Locate every blood parasite and identify its species.
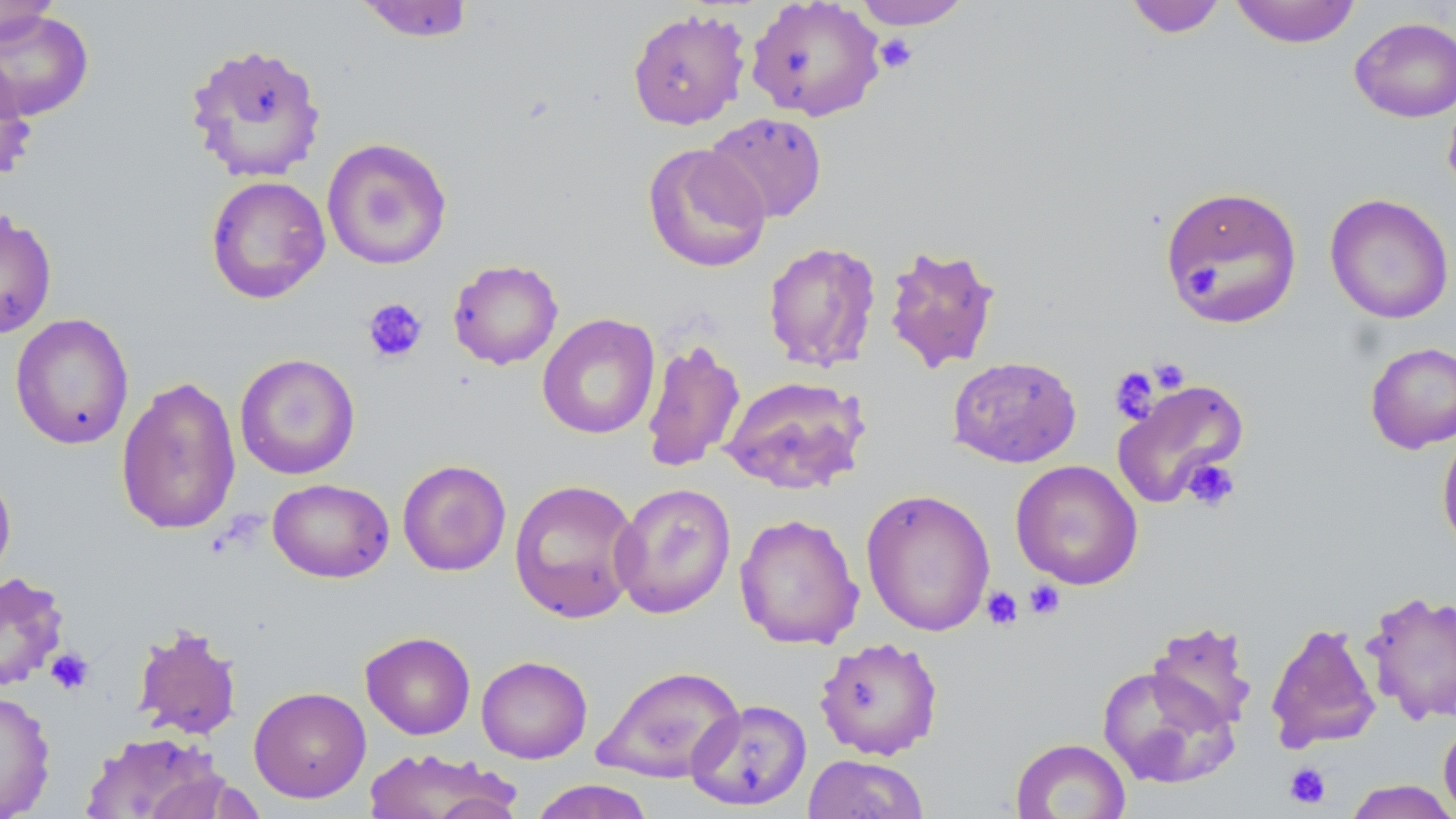

No blood parasites observed.

Summary:
  - Coordinate format: approximate bounding boxes as [x1, y1, x2, y2] in pixels
  - Platelet locations: [874, 33, 918, 74], [1183, 263, 1223, 300], [362, 297, 428, 364], [1149, 357, 1191, 394], [1110, 366, 1161, 424], [1181, 458, 1240, 513], [1024, 579, 1066, 620], [982, 586, 1024, 631], [45, 647, 95, 695], [1284, 762, 1331, 809]
  - Uninfected red blood cell locations: [0, 0, 62, 46], [745, 0, 885, 122], [853, 0, 972, 29], [1124, 0, 1228, 38], [1230, 0, 1361, 48], [355, 1, 477, 42], [0, 8, 95, 122], [627, 8, 751, 130], [1350, 16, 1456, 122], [183, 41, 327, 184], [0, 57, 36, 182], [1442, 92, 1456, 200], [704, 111, 828, 223], [321, 136, 453, 271], [642, 142, 772, 274], [205, 175, 331, 305], [1159, 185, 1303, 328], [1325, 193, 1454, 324], [0, 210, 58, 339], [762, 241, 882, 372], [882, 242, 1001, 374], [448, 259, 563, 370], [10, 313, 134, 450], [537, 313, 659, 440], [640, 337, 746, 474], [1365, 341, 1456, 453], [234, 353, 361, 480], [947, 356, 1082, 468], [720, 375, 871, 495], [115, 376, 241, 535], [1112, 378, 1251, 509], [1436, 426, 1456, 554], [397, 459, 511, 576], [1010, 460, 1143, 590], [0, 464, 16, 585], [268, 478, 394, 583], [509, 478, 641, 624], [610, 482, 736, 619], [860, 488, 996, 637], [734, 512, 864, 650], [1, 571, 69, 692], [1361, 589, 1456, 726], [1146, 620, 1257, 733], [1265, 621, 1381, 753], [131, 624, 242, 740], [360, 631, 476, 739], [814, 637, 944, 761], [476, 655, 592, 763], [592, 664, 745, 783], [1096, 664, 1238, 789], [249, 686, 371, 803], [0, 689, 56, 819], [687, 698, 812, 811], [1438, 718, 1456, 819], [80, 731, 227, 818], [1010, 738, 1131, 819], [362, 747, 521, 818], [803, 753, 930, 818], [528, 779, 656, 819], [1343, 780, 1456, 818]
  - Slide-level diagnosis: no evidence of blood parasites
  - Preparation: thin blood smear
  - Image size: 1456×819 pixels
  - Modality: light microscopy
  - Field of view: single
  - Stain: May-Grünwald-Giemsa
  - Magnification: 1000x